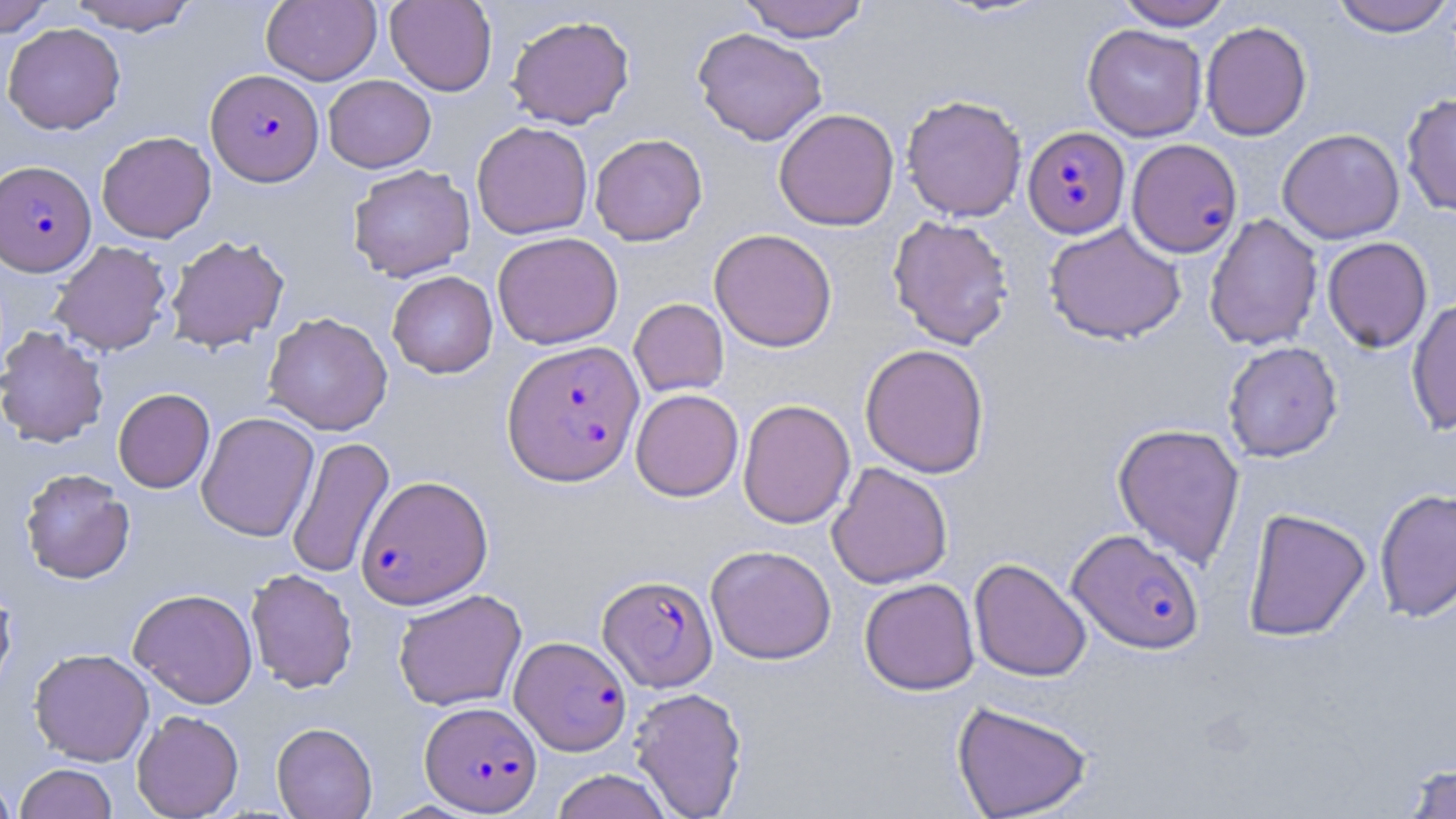

{
  "slide_level_diagnosis": "Plasmodium falciparum",
  "modality": "optical microscopy",
  "plasmodium_falciparum_infected_red_blood_cell_locations": "approximate bounding boxes as (x1,y1)-(x2,y2) corner pairs in pixels: (206,68)-(324,186), (1022,126)-(1130,238), (1126,139)-(1243,258), (0,160)-(96,276), (502,340)-(644,486), (356,475)-(493,609), (1068,529)-(1204,654), (599,574)-(718,692), (510,636)-(632,755), (421,701)-(542,815)",
  "image_size": "1456×819 pixels",
  "stain": "May-Grünwald-Giemsa",
  "uninfected_red_blood_cell_locations": "approximate bounding boxes as (x1,y1)-(x2,y2) corner pairs in pixels: (66,0)-(199,35), (262,0)-(381,85), (384,0)-(497,96), (737,0)-(871,42), (1115,0)-(1234,30), (1328,0)-(1455,37), (0,1)-(56,37), (506,14)-(635,128), (2,22)-(126,135), (1200,22)-(1312,141), (1083,23)-(1207,141), (692,27)-(828,146), (323,75)-(436,172), (1401,92)-(1456,215), (901,93)-(1027,221), (773,108)-(900,232), (471,121)-(593,239), (1278,128)-(1404,244), (97,131)-(216,243), (590,133)-(708,245), (348,164)-(475,282), (887,214)-(1015,350), (1204,214)-(1323,351), (1044,222)-(1186,344), (709,228)-(838,352), (492,231)-(623,349), (165,234)-(289,353), (1322,237)-(1432,353), (49,240)-(172,356), (386,271)-(498,378), (1406,297)-(1456,435), (629,298)-(729,397), (263,312)-(393,436), (0,325)-(109,448), (1222,341)-(1343,462), (860,344)-(990,478), (113,388)-(215,493), (631,388)-(744,501), (737,399)-(856,529), (196,412)-(319,541), (1112,422)-(1246,570), (287,435)-(395,580), (827,462)-(953,589), (19,468)-(135,584), (1374,487)-(1456,622), (1242,507)-(1371,642), (706,544)-(836,665), (969,558)-(1092,682), (245,569)-(358,692), (0,575)-(18,699), (859,578)-(980,695), (128,588)-(258,708), (393,588)-(527,712), (29,648)-(154,766), (628,686)-(748,818), (951,700)-(1094,819), (131,709)-(244,818), (271,722)-(378,818), (1399,761)-(1456,818), (14,763)-(117,819), (550,769)-(674,819), (0,771)-(17,819)",
  "field_of_view": "single",
  "magnification": "1000x",
  "preparation": "thin blood smear"
}